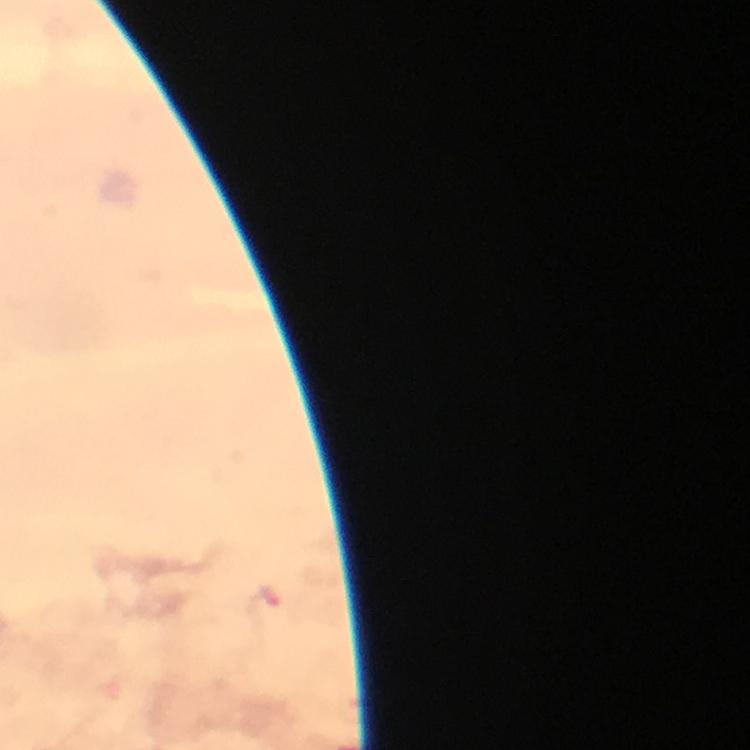

Approximate centers as {x, y} in pixels. Plasmodium parasite locations: {267, 602}. Photographed with a smartphone mounted on the microscope. Image is 750×750 pixels. Giemsa stain. Immersion oil was used. Cropped region of a single field of view. 100x magnification. Thick smear. From a diagnostic examination for malaria.